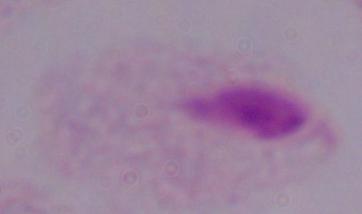

identification: trichomonad
magnification: 1000x
modality: photomicrograph